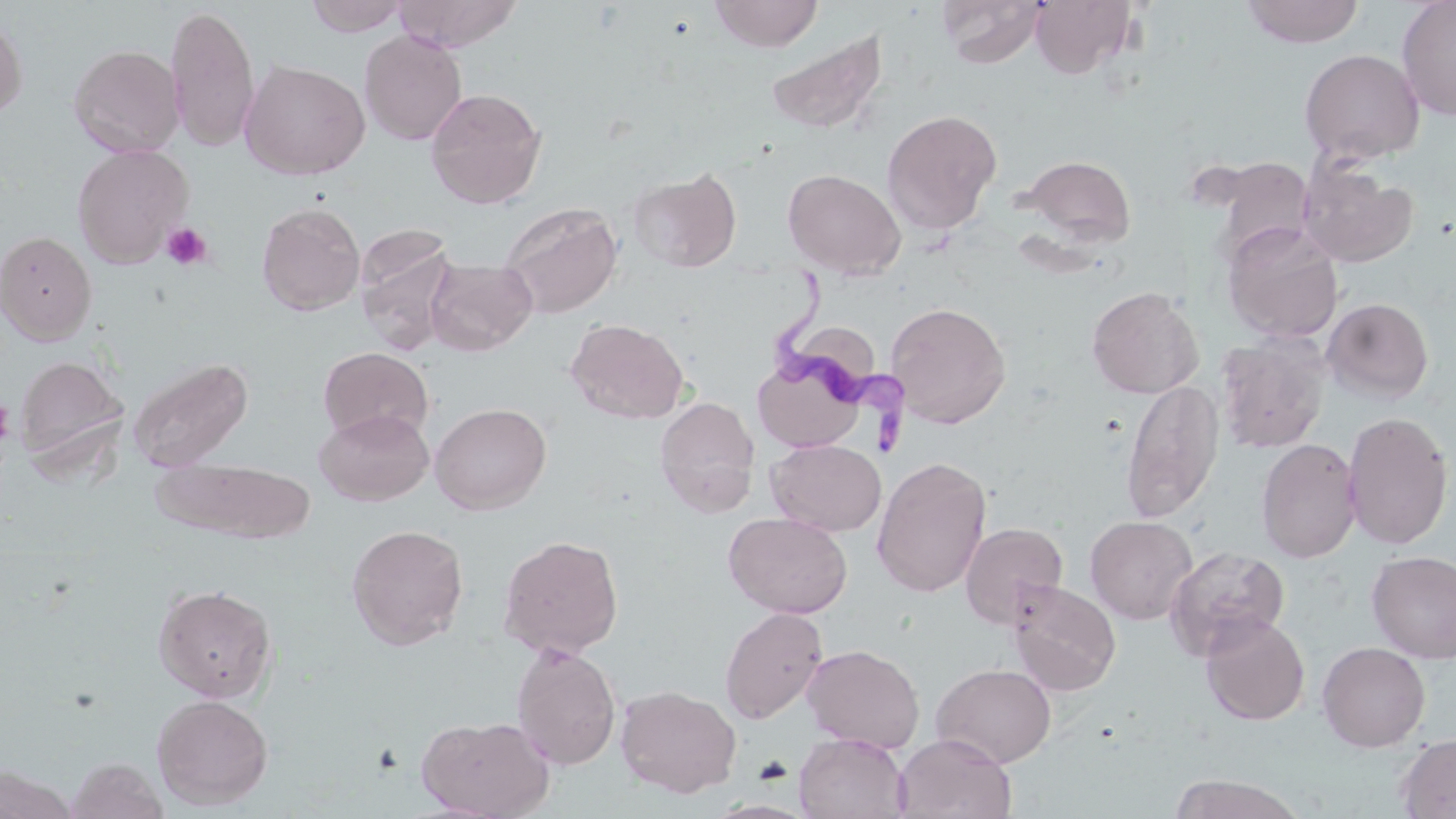
Approximate bounding boxes as (x1, y1, x2, y2) in pixels. Trypanosoma brucei locations: (771, 279, 913, 460). Platelet locations: (160, 221, 214, 271), (1, 395, 13, 453). Uninfected red blood cell locations: (303, 0, 412, 37), (392, 0, 524, 52), (709, 0, 824, 52), (936, 0, 1047, 68), (1029, 0, 1137, 79), (1240, 0, 1365, 48), (1396, 0, 1456, 121), (164, 5, 259, 151), (0, 12, 28, 121), (359, 29, 468, 145), (764, 30, 889, 135), (68, 44, 185, 158), (1299, 48, 1425, 164), (239, 59, 371, 180), (425, 87, 547, 209), (881, 110, 1002, 236), (72, 144, 193, 269), (1019, 154, 1136, 248), (1299, 161, 1418, 268), (628, 167, 742, 273), (782, 168, 906, 279), (499, 201, 623, 318), (256, 202, 366, 316), (1222, 223, 1344, 343), (354, 227, 460, 356), (0, 230, 97, 345), (426, 258, 537, 356), (1086, 286, 1204, 398), (1322, 296, 1434, 403), (885, 301, 1012, 428), (565, 317, 689, 424), (1217, 334, 1330, 453), (318, 347, 433, 444), (751, 350, 873, 453), (15, 354, 129, 466), (127, 356, 254, 474), (1121, 379, 1224, 523), (653, 396, 759, 516), (429, 402, 552, 515), (315, 408, 434, 505), (1341, 410, 1453, 550), (767, 439, 885, 536), (1256, 439, 1362, 563), (871, 456, 992, 597), (155, 457, 315, 542), (724, 512, 852, 619), (1085, 515, 1197, 624), (959, 522, 1068, 628), (346, 523, 469, 650), (497, 534, 624, 658), (1166, 546, 1293, 666), (1366, 550, 1456, 663), (1007, 580, 1122, 695), (153, 583, 277, 702), (719, 606, 828, 724), (1199, 614, 1310, 726), (1317, 641, 1431, 752), (511, 642, 622, 770), (802, 644, 924, 752), (932, 663, 1057, 767), (615, 684, 742, 798), (151, 694, 273, 810), (416, 714, 556, 818), (794, 733, 910, 819), (893, 733, 1017, 818), (1396, 733, 1456, 819), (66, 757, 168, 819), (0, 766, 78, 819), (1169, 774, 1305, 818). Slide-level diagnosis: Trypanosoma brucei. 1000x magnification. May-Grünwald-Giemsa-stained preparation. One field of a larger specimen. Thin blood smear. Optical microscopy. Image is 1456×819 pixels.